Report the malaria status of this cell.
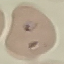

It is parasitized.

preparation = thin blood film
stain = Giemsa
capture = smartphone through the microscope eyepiece
image type = cell patch, automatically extracted from a larger field of view and resized to 64 × 64 pixels